Assess the morphology of the erythrocytes.
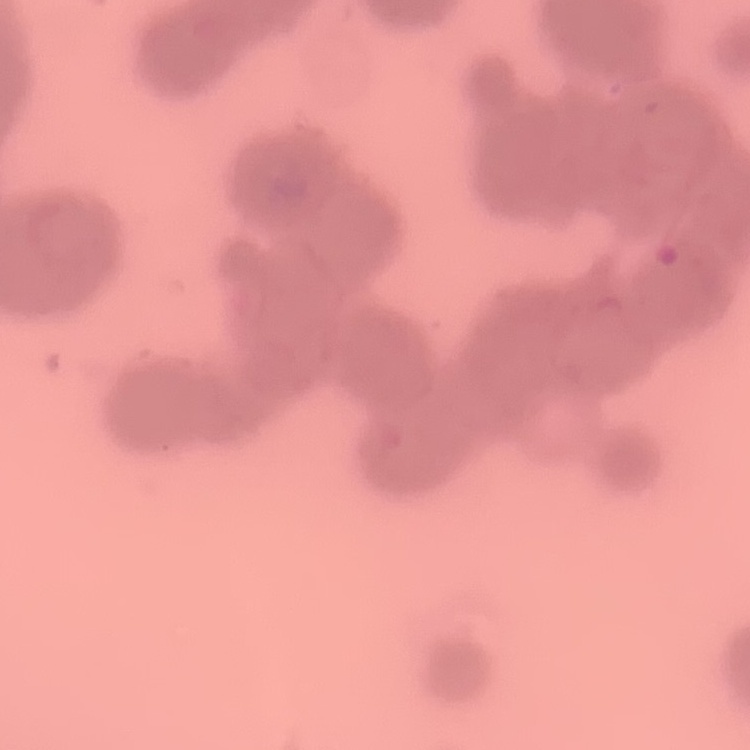
Rouleaux formation.

Stained with either Field's or Giemsa. Thin peripheral smear. Square crop of a larger photomicrograph.